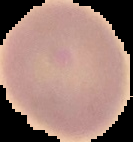
Summary:
  - Image size: 133×142 pixels
  - Malaria status: uninfected
  - Image type: segmented cell region on a black background
  - Preparation: thin blood smear